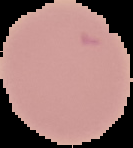
image size = 133×148 pixels
malaria status = uninfected
preparation = thin blood smear
image type = segmented cell region with the area outside set to black